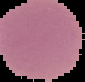

image size = 85×82 pixels
preparation = thin blood film
result = no malaria parasites detected
image type = cell region segmented out of the field of view; surrounding area masked to black